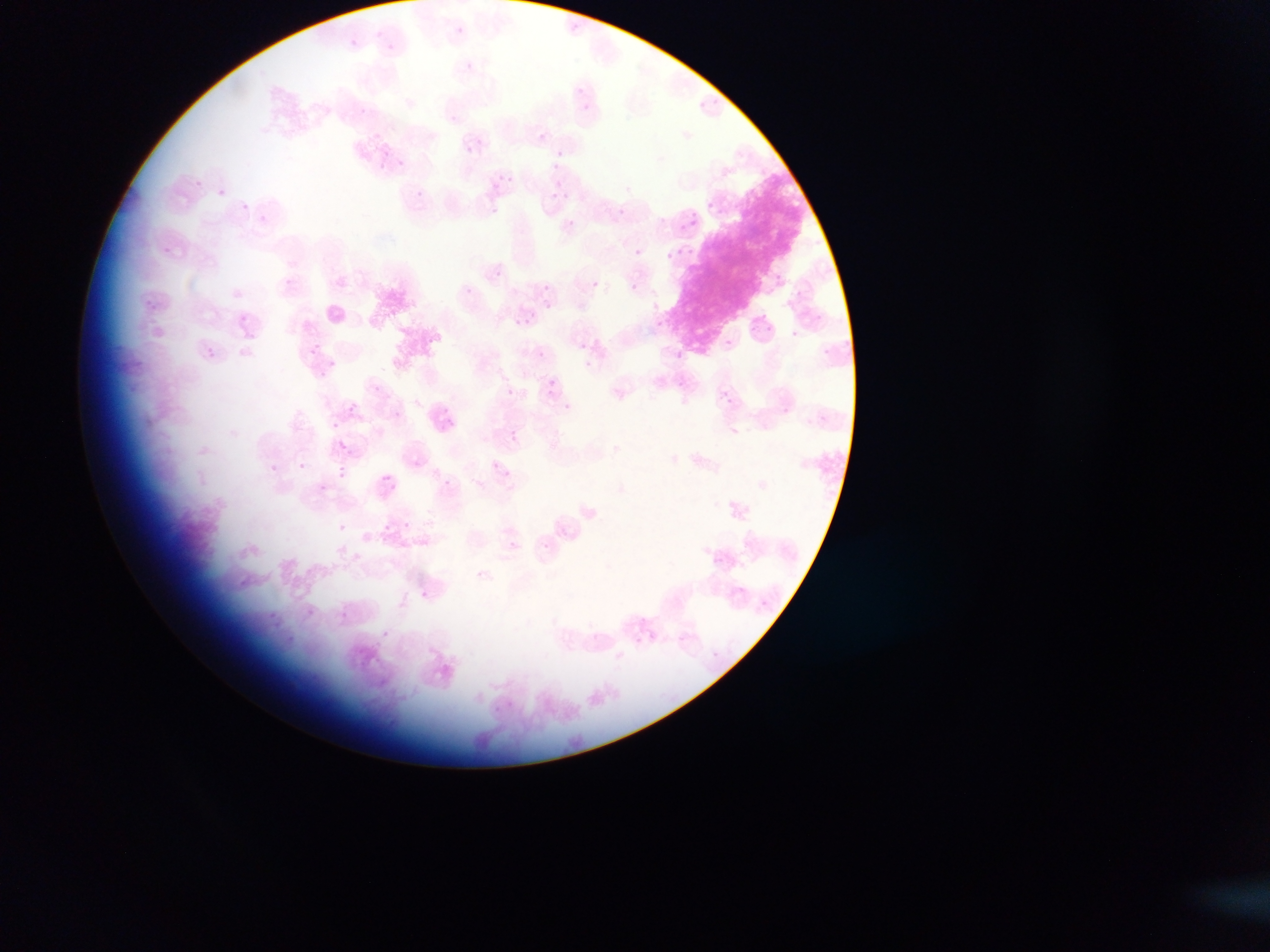
Approximate bounding boxes as (left, top, right, bottom) in pixels.
Summary:
  - Plasmodium parasite locations: (465, 63, 473, 71), (700, 101, 709, 112), (450, 114, 458, 122), (539, 132, 547, 141), (465, 146, 474, 154), (396, 159, 404, 167), (505, 173, 512, 181), (550, 173, 568, 189), (193, 179, 204, 192), (493, 181, 501, 189), (217, 189, 225, 196), (547, 189, 571, 200), (703, 200, 725, 222), (241, 204, 249, 212), (619, 207, 627, 215), (690, 210, 699, 225), (258, 215, 266, 222), (564, 215, 579, 235), (675, 221, 688, 233), (163, 245, 172, 258), (634, 248, 643, 257), (662, 253, 685, 267), (492, 266, 503, 282), (776, 276, 784, 284), (284, 277, 292, 285), (591, 280, 599, 288), (631, 285, 639, 293), (542, 286, 550, 293), (463, 287, 477, 299), (141, 297, 158, 311), (546, 301, 554, 308), (238, 311, 258, 328), (760, 311, 768, 318), (509, 315, 529, 329), (657, 316, 672, 338), (723, 340, 732, 348), (202, 341, 217, 358), (307, 341, 324, 364), (580, 341, 588, 350), (537, 347, 545, 355), (674, 348, 683, 358), (328, 359, 336, 367), (676, 378, 684, 388), (547, 380, 556, 389), (373, 385, 381, 393), (505, 387, 514, 395), (722, 391, 731, 401), (723, 395, 731, 404), (348, 404, 356, 412), (331, 420, 339, 428), (510, 431, 518, 440), (337, 441, 347, 450), (298, 462, 305, 470), (491, 463, 499, 470), (270, 464, 278, 473), (338, 470, 347, 478), (382, 474, 391, 481), (445, 479, 453, 486), (318, 483, 326, 490), (403, 521, 411, 529), (338, 523, 346, 531), (383, 523, 390, 531), (509, 542, 516, 550), (540, 542, 548, 549), (422, 586, 434, 603), (342, 606, 353, 621), (266, 608, 284, 628), (638, 617, 646, 624), (382, 631, 390, 638), (285, 636, 308, 653), (507, 699, 516, 707) | approximate (x, y) pixel centers of objects too small to bound: (459, 30), (390, 46), (581, 89), (585, 107), (361, 113), (558, 153), (419, 193), (770, 328), (795, 334), (568, 407), (730, 503), (716, 558), (741, 590), (764, 603), (311, 611), (716, 655)
  - Field of view: single
  - Image size: 1270×952 pixels
  - Preparation: thin blood smear
  - Country: Ghana
  - Capture: mobile-phone photograph through a microscope